Outline each blood parasite and name the species.
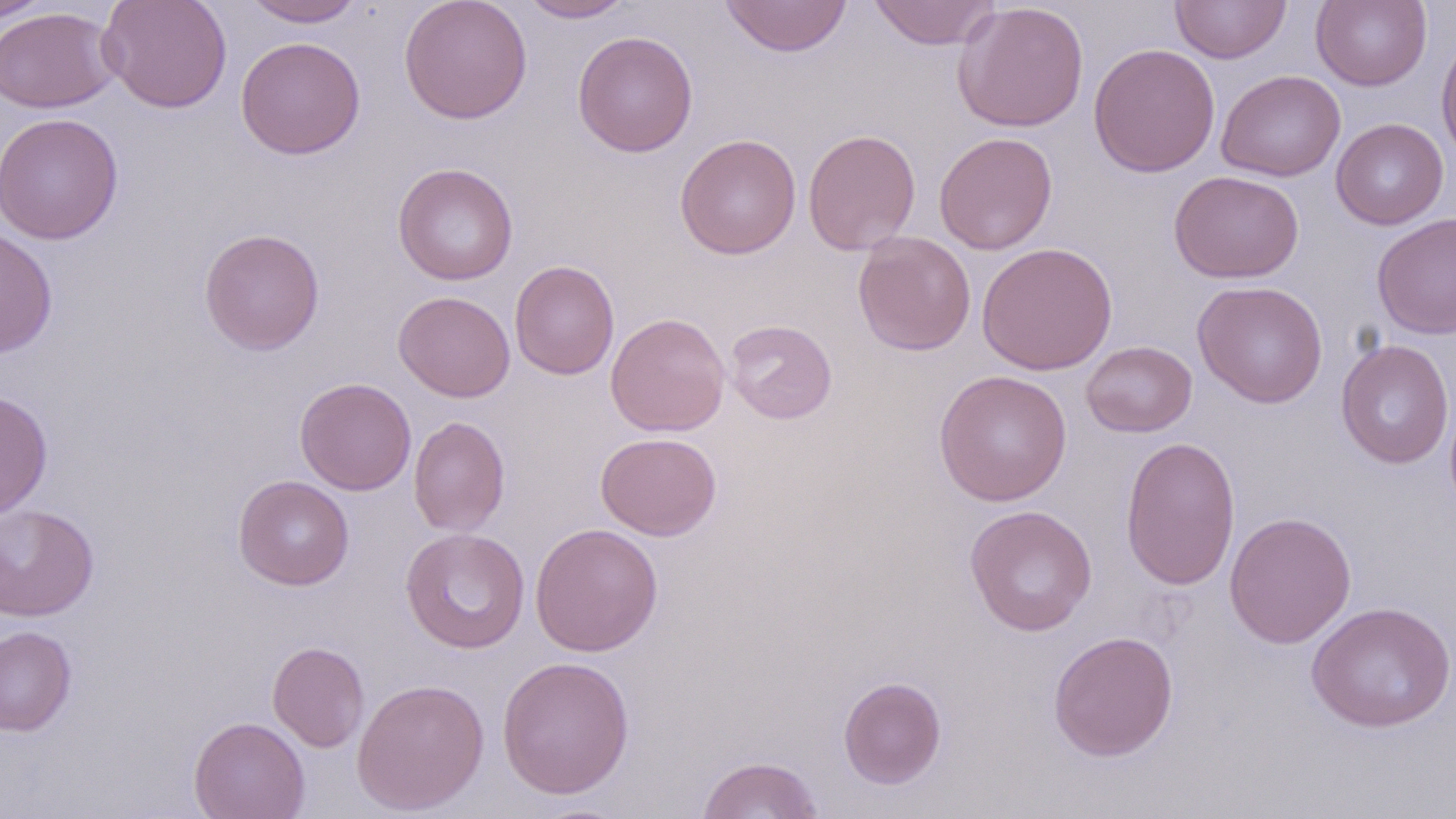

No blood parasites observed.

slide_level_diagnosis: negative for blood parasites
uninfected_red_blood_cell_locations: 'approximate bounding boxes as (x1, y1, x2, y2) in pixels: (0, 0, 56, 23), (98, 0, 233, 114), (241, 0, 366, 28), (399, 0, 532, 125), (519, 0, 635, 23), (719, 0, 852, 57), (868, 0, 1001, 50), (1170, 0, 1291, 64), (1311, 0, 1432, 91), (952, 1, 1089, 132), (0, 6, 119, 113), (572, 31, 698, 157), (1436, 32, 1456, 167), (235, 35, 366, 159), (1088, 42, 1220, 178), (1216, 69, 1345, 182), (0, 113, 125, 244), (1330, 118, 1448, 230), (802, 128, 921, 255), (934, 132, 1058, 255), (675, 133, 802, 259), (392, 162, 518, 286), (1169, 170, 1304, 283), (1371, 212, 1456, 340), (0, 227, 58, 357), (198, 228, 325, 355), (853, 232, 976, 356), (977, 242, 1117, 375), (509, 260, 619, 379), (1192, 280, 1328, 408), (393, 290, 516, 403), (605, 312, 731, 437), (724, 319, 837, 424), (1335, 339, 1455, 469), (1081, 341, 1197, 438), (934, 369, 1073, 507), (295, 377, 416, 496), (0, 391, 53, 519), (408, 415, 510, 536), (595, 432, 722, 541), (1120, 435, 1240, 591), (233, 475, 354, 590), (0, 503, 99, 622), (964, 505, 1097, 636), (1224, 511, 1357, 649), (530, 522, 664, 657), (400, 527, 530, 654), (1306, 601, 1455, 732), (0, 625, 77, 736), (1048, 630, 1179, 762), (267, 641, 369, 753), (496, 654, 635, 800), (838, 675, 947, 789), (351, 677, 490, 815), (189, 716, 310, 819), (697, 755, 825, 818)'
preparation: thin blood smear
modality: light microscopy
image_size: 1456×819 pixels
field_of_view: single
stain: May-Grünwald-Giemsa
magnification: 1000x